State which parasite is depicted.
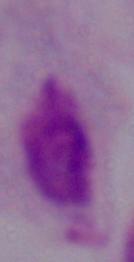

This is a trichomonad.

Summary:
  - Modality: micrograph
  - Magnification: 1000x